Identify the parasite.
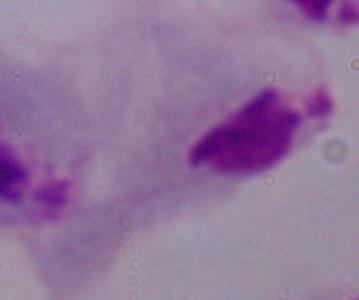

A trichomonad.

Summary:
  - Modality: photomicrograph
  - Magnification: 1000x